Report the malaria status of this cell.
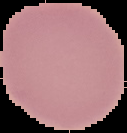

It is uninfected.

Summary:
  - Preparation: thin blood smear
  - Image size: 127×133 pixels
  - Image type: cell region segmented out of the field of view; surrounding area masked to black